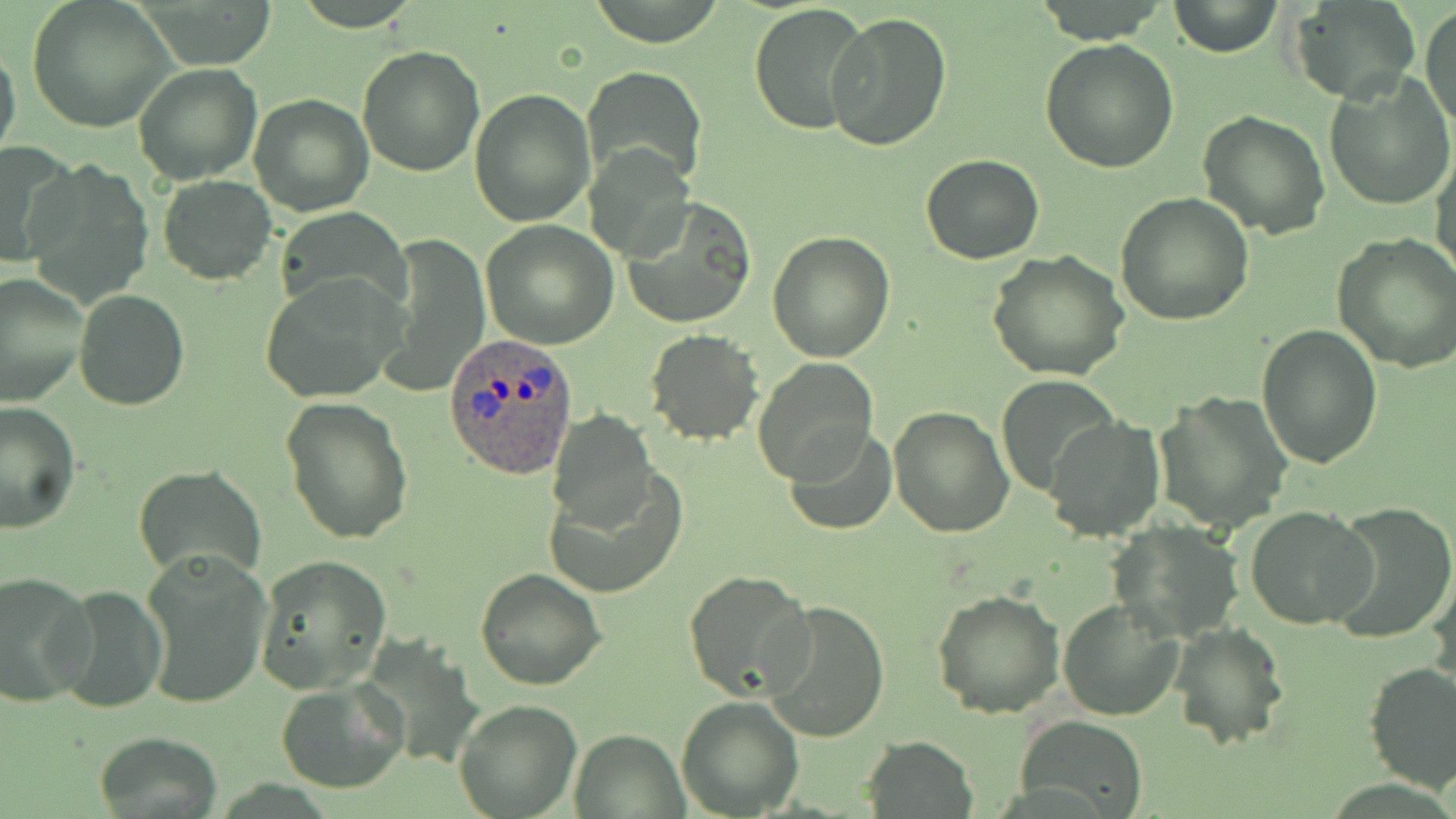
slide_level_diagnosis: Plasmodium ovale
preparation: thin blood smear
image_size: 1456×819 pixels
uninfected_red_blood_cell_locations: 'approximate bounding boxes as [x1, y1, x2, y2] in pixels: [25, 0, 172, 133], [1169, 1, 1281, 56], [749, 3, 872, 135], [1290, 5, 1418, 106], [1421, 6, 1455, 133], [826, 11, 952, 152], [0, 35, 22, 170], [1041, 38, 1179, 174], [358, 44, 486, 177], [133, 63, 261, 185], [582, 64, 706, 192], [1325, 77, 1454, 211], [133, 80, 374, 202], [469, 89, 596, 227], [249, 94, 374, 217], [1197, 111, 1330, 239], [0, 140, 79, 267], [585, 143, 696, 262], [1431, 151, 1455, 283], [919, 153, 1044, 265], [20, 156, 155, 306], [157, 175, 277, 286], [1114, 192, 1255, 326], [623, 198, 757, 330], [275, 210, 413, 320], [480, 220, 619, 348], [766, 229, 895, 361], [376, 233, 489, 399], [1332, 234, 1456, 374], [987, 249, 1130, 381], [0, 273, 88, 407], [261, 275, 407, 405], [73, 289, 192, 411], [1256, 324, 1382, 470], [643, 328, 763, 446], [751, 357, 878, 484], [997, 375, 1120, 499], [1155, 392, 1291, 530], [282, 396, 414, 544], [0, 400, 81, 535], [889, 406, 1014, 537], [547, 408, 662, 528], [1044, 416, 1163, 542], [787, 428, 895, 536], [133, 463, 269, 587], [1324, 504, 1454, 641], [1245, 506, 1375, 631], [1107, 521, 1244, 642], [139, 545, 273, 711], [255, 554, 391, 694], [1428, 558, 1455, 689], [475, 567, 605, 691], [683, 568, 815, 704], [0, 571, 95, 705], [53, 585, 167, 712], [932, 590, 1063, 718], [761, 598, 891, 742], [1057, 598, 1182, 722], [1168, 620, 1289, 748], [1363, 660, 1456, 793], [274, 680, 409, 795], [676, 696, 804, 817], [453, 700, 583, 819], [1015, 714, 1148, 816], [93, 731, 223, 819], [573, 732, 686, 817], [861, 735, 977, 818]'
field_of_view: single
plasmodium_ovale_infected_red_blood_cell_locations: 'approximate bounding boxes as [x1, y1, x2, y2] in pixels: [441, 331, 579, 480]'
modality: optical microscopy
magnification: 1000x
stain: May-Grünwald-Giemsa